Assess this cell for malaria.
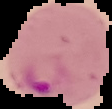

It is parasitized.

image size = 112×109 pixels
preparation = thin blood smear
image type = cell region segmented out of the field of view; surrounding area masked to black